Assess this cell for malaria.
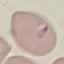
It is parasitized.

image type = cell patch, automatically extracted from a larger field of view and resized to 64 × 64 pixels
preparation = thin smear
stain = Giemsa
capture = smartphone camera at the microscope eyepiece